Classify this cell by malaria status.
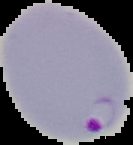

Parasitized.

From a thin blood smear. Cell region segmented out of the field of view; the surrounding area is masked to black. Image is 133×145 pixels.